Outline each Plasmodium ovale-infected red blood cell.
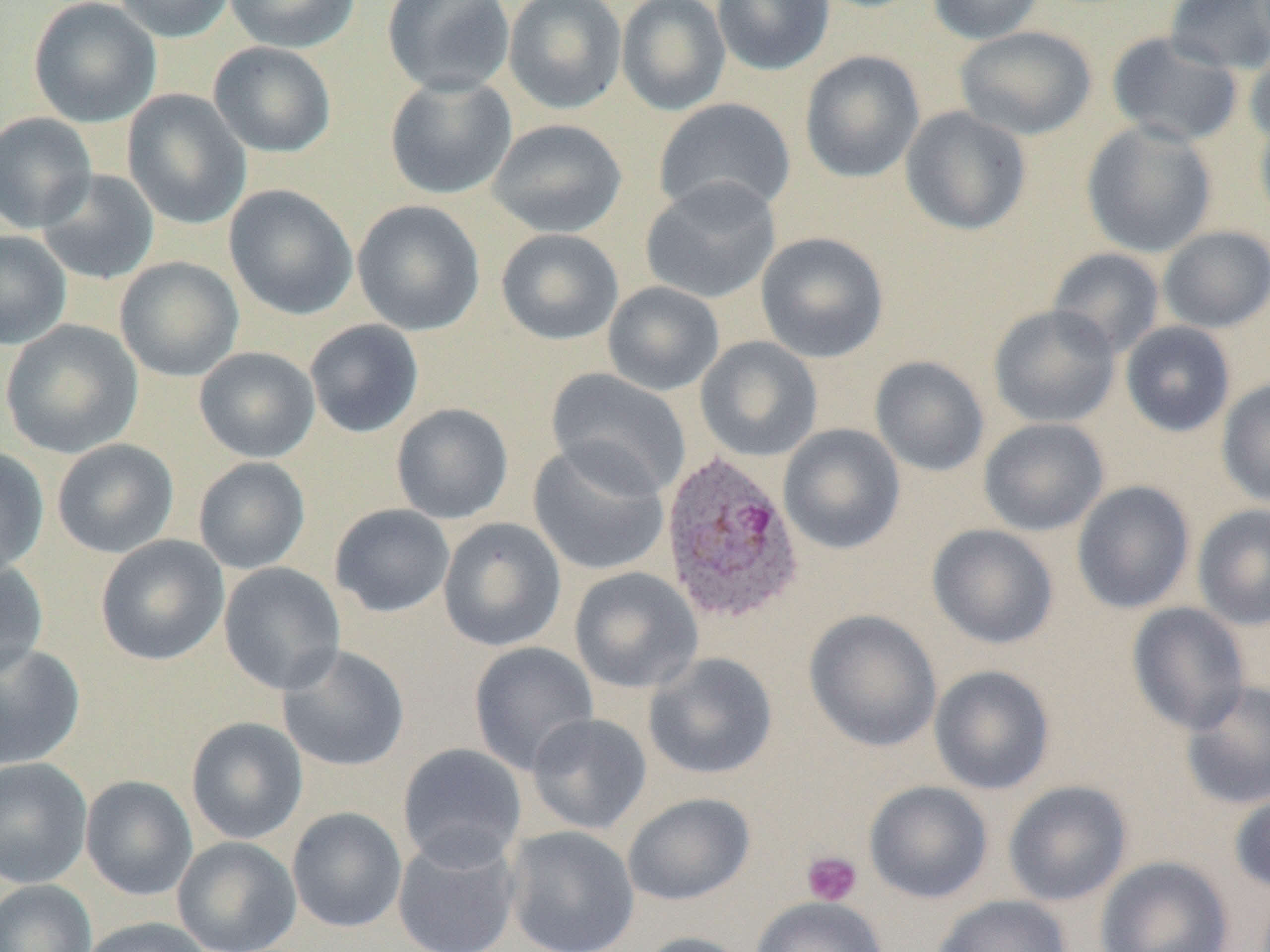

Approximate bounding boxes as [x1, y1, x2, y2] in pixels.
Plasmodium ovale-infected red blood cells: [659, 449, 805, 626].

slide_level_diagnosis: Plasmodium ovale
field_of_view: single
modality: optical microscopy
magnification: 1000x
uninfected_red_blood_cell_locations: 'approximate bounding boxes as [x1, y1, x2, y2] in pixels: [27, 0, 162, 128], [112, 0, 236, 43], [223, 0, 361, 53], [382, 0, 515, 96], [503, 0, 627, 115], [616, 0, 731, 116], [712, 0, 835, 75], [927, 0, 1046, 44], [1164, 0, 1270, 75], [956, 25, 1096, 140], [1106, 31, 1243, 147], [208, 41, 337, 158], [1245, 43, 1270, 149], [799, 50, 925, 184], [384, 73, 517, 200], [122, 89, 252, 230], [653, 98, 797, 219], [900, 105, 1032, 236], [0, 112, 97, 233], [1254, 112, 1270, 234], [486, 118, 628, 238], [1081, 120, 1218, 258], [36, 168, 160, 285], [639, 177, 782, 305], [224, 184, 358, 320], [352, 200, 485, 336], [1158, 226, 1270, 333], [496, 229, 624, 345], [0, 230, 72, 350], [755, 232, 890, 363], [1047, 247, 1166, 359], [114, 256, 245, 382], [602, 281, 725, 396], [988, 304, 1121, 429], [304, 319, 424, 438], [1, 320, 143, 459], [1120, 321, 1236, 438], [694, 336, 823, 463], [194, 346, 320, 463], [869, 355, 990, 477], [545, 368, 691, 499], [1217, 378, 1270, 509], [391, 403, 513, 525], [978, 418, 1110, 536], [778, 423, 905, 554], [51, 438, 179, 558], [527, 440, 671, 577], [0, 446, 49, 577], [193, 457, 310, 574], [1071, 481, 1195, 614], [1193, 503, 1270, 630], [330, 504, 455, 618], [438, 517, 567, 652], [927, 524, 1059, 650], [95, 535, 229, 665], [0, 558, 48, 679], [218, 562, 346, 695], [569, 566, 703, 694], [1127, 602, 1251, 734], [804, 609, 942, 752], [468, 641, 599, 775], [0, 642, 85, 769], [277, 644, 410, 772], [642, 652, 778, 780], [929, 665, 1055, 795], [1180, 681, 1270, 810], [526, 713, 652, 835], [186, 717, 308, 845], [397, 742, 528, 869], [0, 757, 93, 888], [80, 775, 198, 901], [864, 780, 993, 904], [1003, 780, 1133, 906], [1229, 787, 1270, 894], [622, 792, 756, 906], [287, 807, 407, 933], [505, 826, 639, 952], [392, 833, 521, 952], [172, 836, 302, 952], [1095, 856, 1234, 951], [0, 879, 96, 952], [932, 895, 1073, 952], [751, 896, 888, 952], [80, 917, 213, 952], [634, 932, 752, 952]'
preparation: thin blood film
image_size: 1270×952 pixels
platelet_locations: 'approximate bounding boxes as [x1, y1, x2, y2] in pixels: [802, 850, 862, 906]'